Give the position of every Plasmodium parasite.
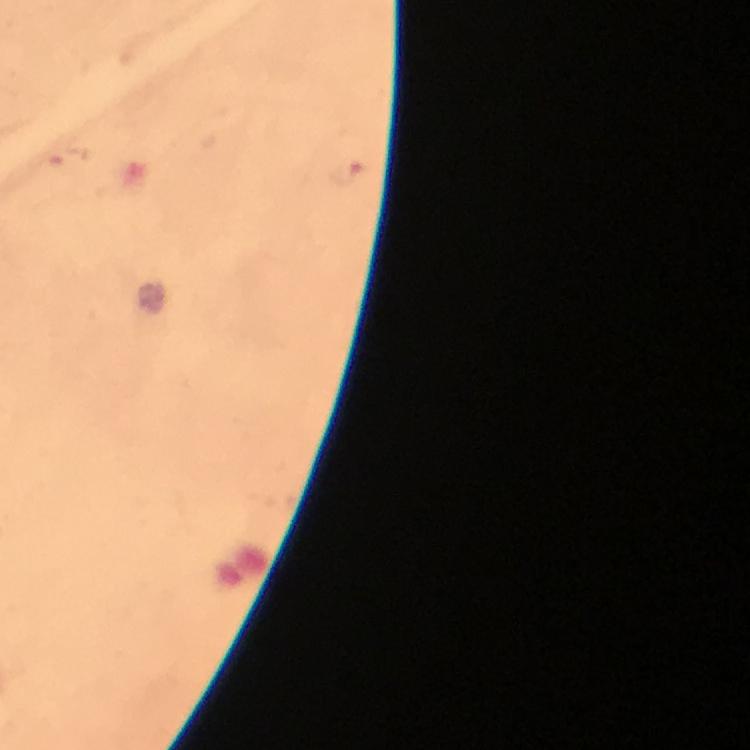
Approximate centers as {x, y} in pixels.
Plasmodium parasites: {69, 156}, {345, 170}.

Summary:
  - Capture: smartphone photograph through a microscope
  - Cropped from: one field of view
  - Context: from a diagnostic examination for malaria
  - Stain: Giemsa
  - Image size: 750×750 pixels
  - Immersion oil: applied
  - Magnification: 100x
  - Preparation: thick blood film